Outline each blood parasite and name the species.
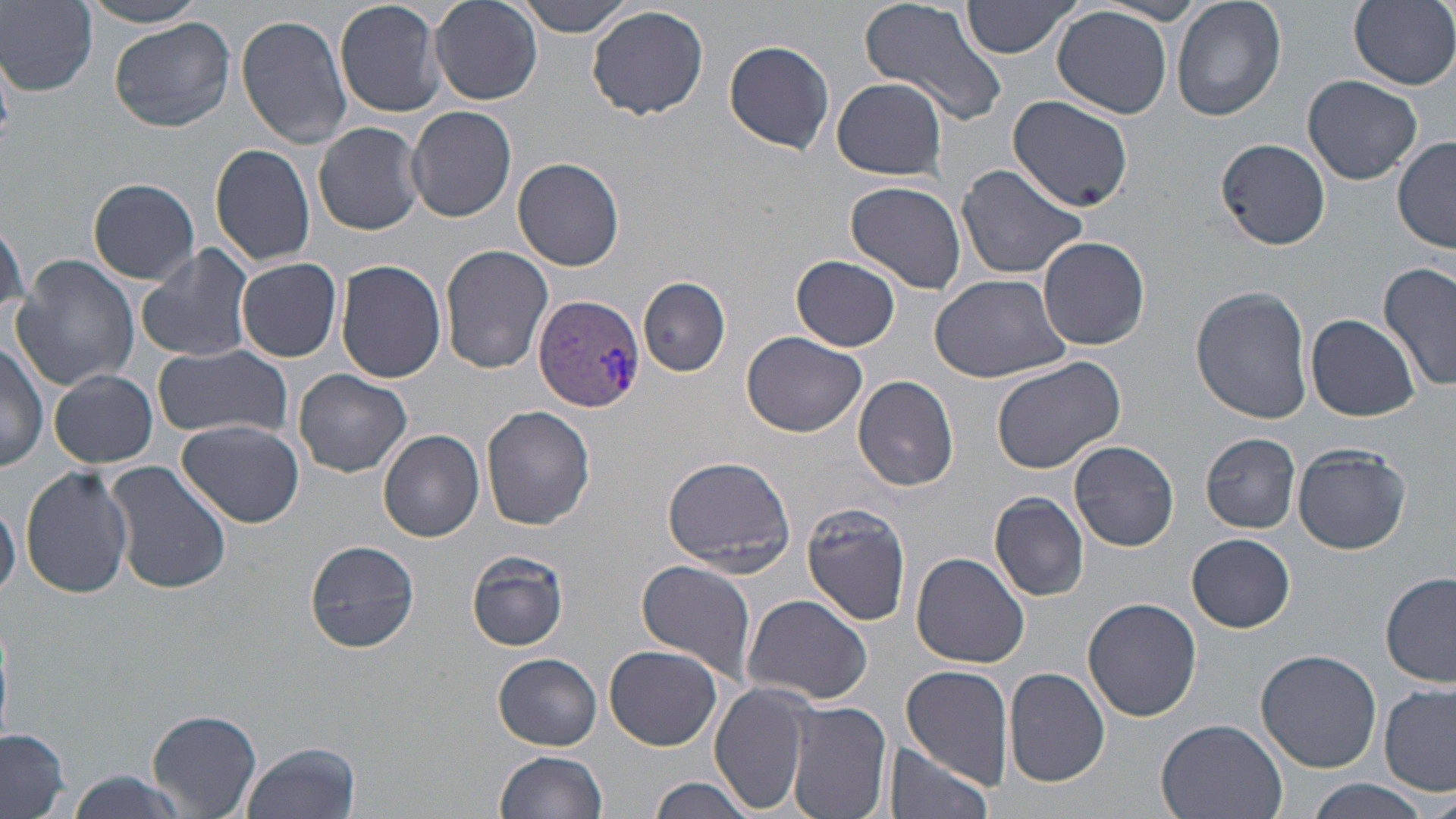

Approximate bounding boxes as named x1/y1/x2/y2 corners in pixels.
Plasmodium vivax-infected red blood cells: (x1=534, y1=294, x2=644, y2=411).
No Plasmodium falciparum, Plasmodium ovale, Plasmodium malariae, Babesia divergens, or Trypanosoma brucei observed.

Summary:
  - Uninfected red blood cell locations: (x1=335, y1=0, x2=446, y2=117), (x1=429, y1=0, x2=541, y2=105), (x1=512, y1=0, x2=638, y2=36), (x1=857, y1=0, x2=1012, y2=128), (x1=962, y1=0, x2=1082, y2=59), (x1=1171, y1=0, x2=1286, y2=122), (x1=1349, y1=0, x2=1456, y2=89), (x1=2, y1=1, x2=98, y2=93), (x1=83, y1=1, x2=213, y2=28), (x1=587, y1=4, x2=709, y2=120), (x1=1052, y1=6, x2=1173, y2=118), (x1=235, y1=15, x2=353, y2=147), (x1=110, y1=18, x2=235, y2=132), (x1=723, y1=40, x2=835, y2=155), (x1=1039, y1=49, x2=1161, y2=197), (x1=1302, y1=75, x2=1424, y2=184), (x1=830, y1=76, x2=948, y2=179), (x1=1007, y1=96, x2=1133, y2=213), (x1=407, y1=105, x2=517, y2=222), (x1=314, y1=121, x2=426, y2=235), (x1=1215, y1=137, x2=1332, y2=249), (x1=1394, y1=137, x2=1456, y2=252), (x1=209, y1=143, x2=317, y2=268), (x1=513, y1=157, x2=623, y2=271), (x1=955, y1=162, x2=1089, y2=279), (x1=88, y1=178, x2=200, y2=284), (x1=846, y1=181, x2=967, y2=294), (x1=1036, y1=237, x2=1150, y2=351), (x1=136, y1=243, x2=256, y2=362), (x1=440, y1=245, x2=554, y2=373), (x1=792, y1=254, x2=900, y2=350), (x1=10, y1=255, x2=140, y2=394), (x1=237, y1=257, x2=344, y2=362), (x1=336, y1=261, x2=447, y2=385), (x1=1379, y1=262, x2=1456, y2=395), (x1=929, y1=273, x2=1072, y2=383), (x1=639, y1=277, x2=730, y2=376), (x1=1190, y1=285, x2=1313, y2=424), (x1=1306, y1=314, x2=1421, y2=421), (x1=742, y1=330, x2=868, y2=438), (x1=0, y1=338, x2=49, y2=474), (x1=153, y1=345, x2=294, y2=443), (x1=989, y1=355, x2=1126, y2=475), (x1=49, y1=368, x2=158, y2=468), (x1=295, y1=370, x2=411, y2=476), (x1=853, y1=375, x2=959, y2=491), (x1=481, y1=405, x2=595, y2=531), (x1=177, y1=419, x2=304, y2=527), (x1=379, y1=429, x2=484, y2=541), (x1=1200, y1=431, x2=1303, y2=531), (x1=1069, y1=438, x2=1179, y2=551), (x1=1291, y1=443, x2=1411, y2=554), (x1=661, y1=457, x2=796, y2=575), (x1=105, y1=461, x2=231, y2=596), (x1=19, y1=464, x2=135, y2=598), (x1=990, y1=492, x2=1090, y2=601), (x1=0, y1=496, x2=20, y2=603), (x1=802, y1=502, x2=913, y2=625), (x1=1187, y1=533, x2=1296, y2=633), (x1=305, y1=538, x2=421, y2=653), (x1=467, y1=550, x2=571, y2=651), (x1=913, y1=552, x2=1031, y2=669), (x1=636, y1=559, x2=757, y2=686), (x1=1380, y1=572, x2=1456, y2=687), (x1=744, y1=595, x2=875, y2=706), (x1=1083, y1=598, x2=1201, y2=722), (x1=603, y1=644, x2=722, y2=751), (x1=1255, y1=649, x2=1381, y2=772), (x1=492, y1=654, x2=603, y2=750), (x1=902, y1=663, x2=1015, y2=787), (x1=1003, y1=667, x2=1112, y2=788), (x1=710, y1=683, x2=814, y2=815), (x1=1378, y1=684, x2=1455, y2=794), (x1=785, y1=700, x2=893, y2=819), (x1=149, y1=709, x2=262, y2=816), (x1=1156, y1=717, x2=1289, y2=819), (x1=0, y1=728, x2=72, y2=817), (x1=241, y1=740, x2=361, y2=818), (x1=884, y1=741, x2=995, y2=819), (x1=494, y1=750, x2=609, y2=819), (x1=647, y1=776, x2=760, y2=819), (x1=1301, y1=781, x2=1434, y2=819)
  - Slide-level diagnosis: Plasmodium vivax
  - Preparation: thin blood smear
  - Image size: 1456×819 pixels
  - Magnification: 1000x
  - Stain: May-Grünwald-Giemsa
  - Modality: light microscopy
  - Field of view: one of a larger specimen